Classify this cell by malaria status.
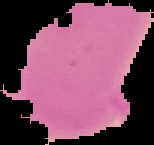

It is uninfected.

preparation = thin blood film
image type = segmented cell region on a black background
image size = 154×145 pixels